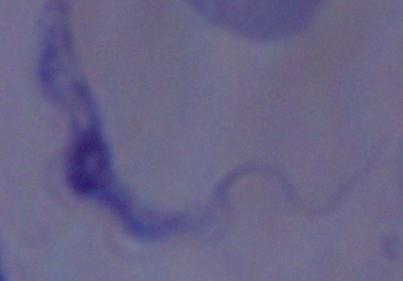

Micrograph. Captured at 1000x magnification. A trypanosome is seen.